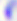

identification = Toxoplasma gondii
modality = photomicrograph
magnification = 400x